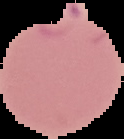
{
  "image_size": "124×139 pixels",
  "image_type": "segmented cell region with the area outside set to black",
  "preparation": "thin blood film",
  "malaria_status": "parasitized"
}